Outline each blood parasite and name the species.
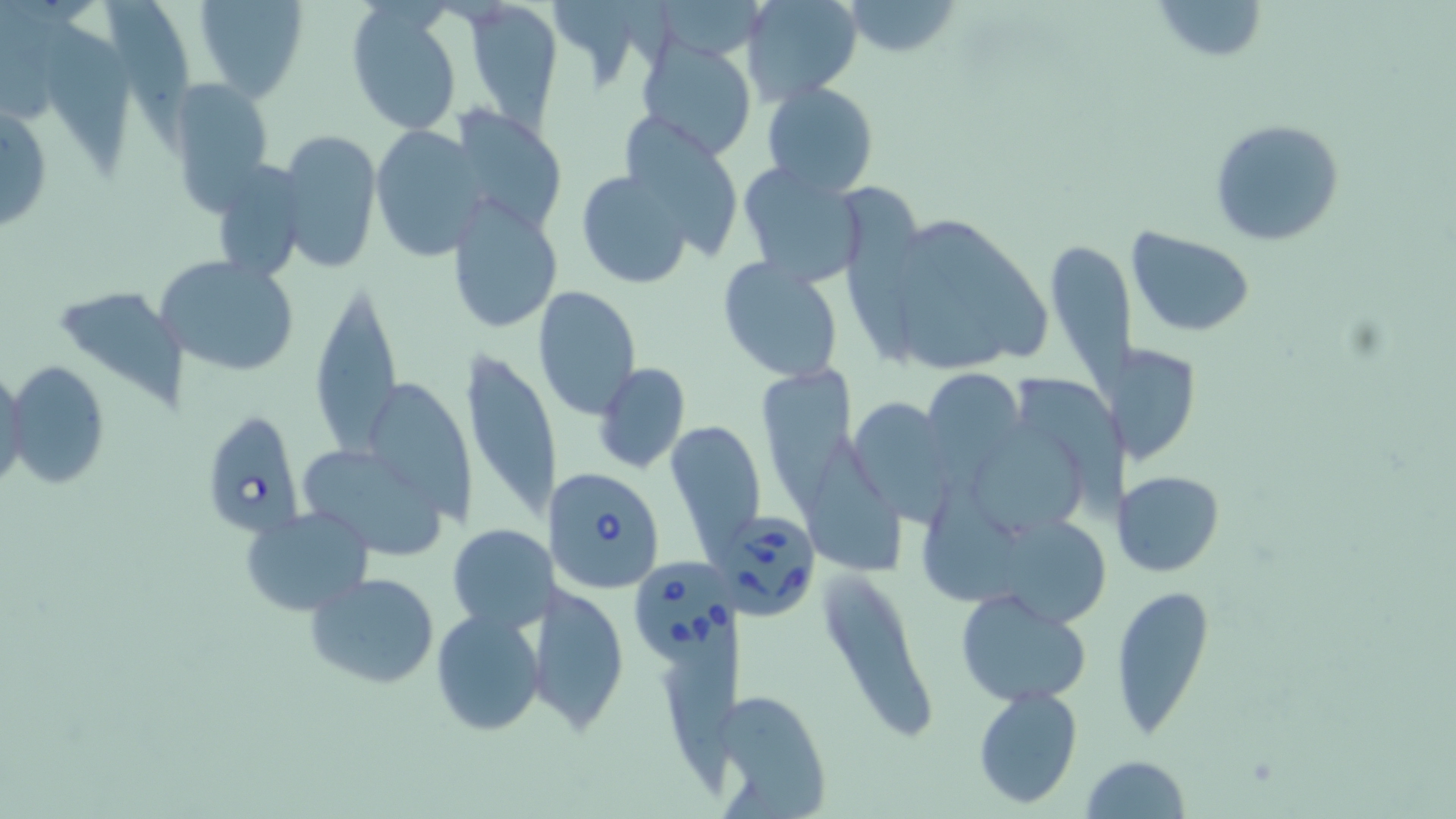

Approximate bounding boxes as (x1,y1)-(x2,y2) corner pairs in pixels.
Babesia divergens-infected red blood cells: (203,412)-(308,540), (552,467)-(666,594), (728,508)-(821,623), (632,557)-(744,670).
No Plasmodium falciparum, Plasmodium ovale, Plasmodium malariae, Plasmodium vivax, or Trypanosoma brucei observed.

slide-level diagnosis = Babesia divergens
uninfected red blood cell locations = approximate bounding boxes as (x1,y1)-(x2,y2) corner pairs in pixels: (193,0)-(310,103), (541,0)-(660,86), (741,0)-(862,103), (1151,0)-(1267,64), (840,1)-(963,57), (100,2)-(196,155), (346,2)-(463,136), (461,3)-(565,127), (37,8)-(138,178), (634,36)-(757,162), (169,77)-(276,212), (761,82)-(879,197), (0,101)-(51,237), (446,107)-(568,233), (627,119)-(740,266), (1209,119)-(1348,248), (371,125)-(485,261), (279,129)-(381,273), (209,161)-(307,284), (736,162)-(866,286), (575,169)-(697,290), (847,190)-(924,362), (446,192)-(563,335), (922,219)-(1049,358), (1126,229)-(1255,338), (890,236)-(1004,371), (1049,238)-(1135,403), (155,254)-(301,379), (717,257)-(843,383), (307,274)-(402,460), (60,287)-(191,410), (533,287)-(640,417), (462,344)-(558,527), (1122,344)-(1200,463), (6,361)-(112,488), (594,362)-(691,475), (761,365)-(854,522), (1,366)-(28,496), (921,367)-(1023,476), (1021,373)-(1136,509), (374,381)-(474,522), (853,398)-(948,526), (667,420)-(764,560), (970,421)-(1088,540), (810,433)-(904,574), (304,449)-(444,555), (1119,470)-(1225,578), (922,473)-(1021,608), (241,505)-(373,616), (1004,521)-(1109,633), (447,523)-(552,634), (303,570)-(441,688), (821,570)-(934,744), (542,578)-(631,736), (1109,583)-(1213,735), (955,588)-(1093,706), (430,608)-(546,737), (656,647)-(755,792), (972,686)-(1082,808), (1081,756)-(1191,818)
magnification = 1000x
field of view = single
preparation = thin blood smear
stain = May-Grünwald-Giemsa
modality = light microscopy
image size = 1456×819 pixels